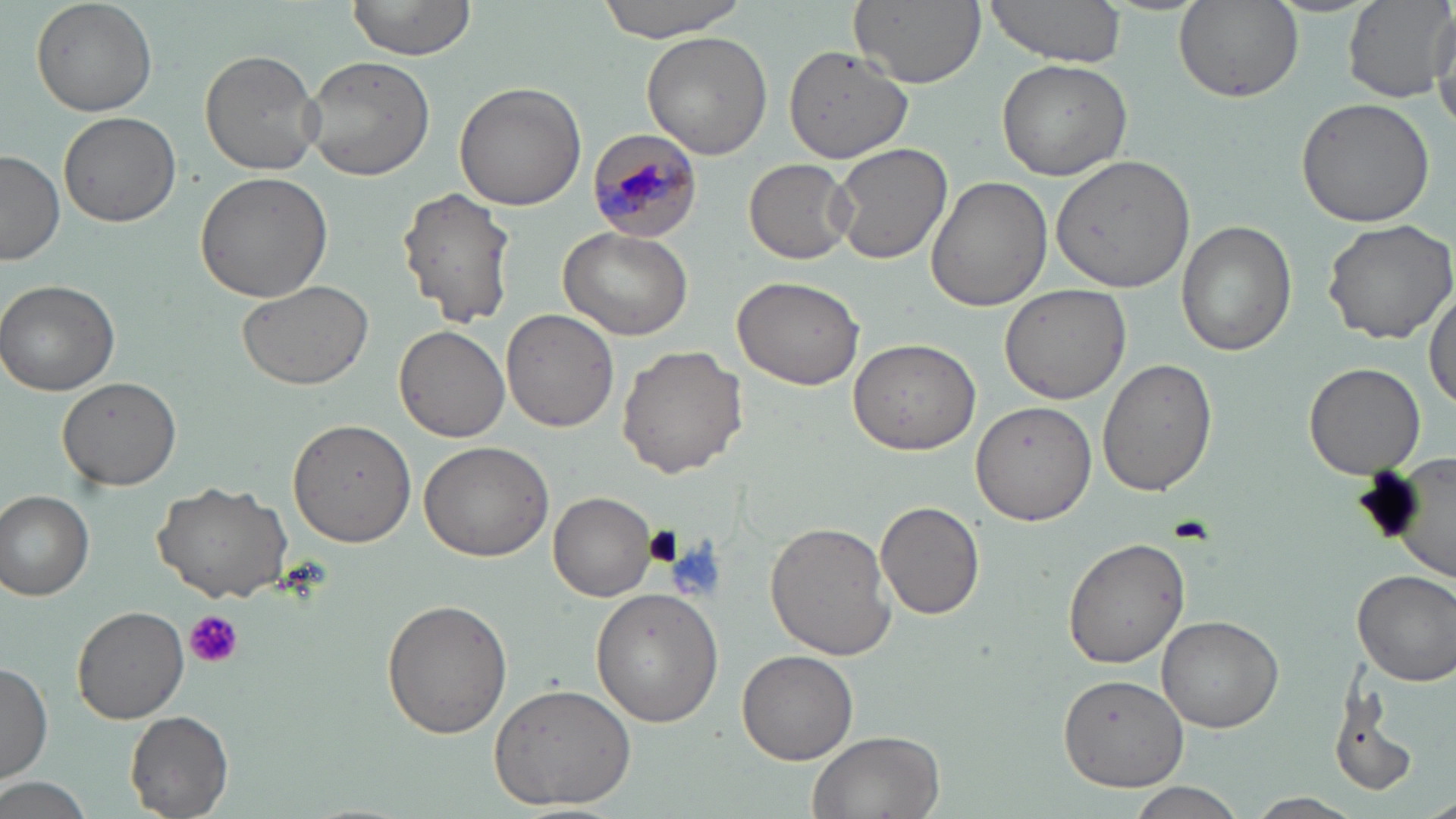

Summary:
  - Coordinate format: approximate bounding boxes as (x1, y1, x2, y2) in pixels
  - Platelet locations: (183, 610, 243, 670)
  - Plasmodium malariae-infected red blood cell locations: (585, 128, 707, 243)
  - Uninfected red blood cell locations: (31, 0, 158, 116), (341, 0, 480, 67), (597, 0, 746, 40), (850, 0, 985, 89), (980, 0, 1129, 66), (1343, 0, 1453, 103), (1174, 1, 1304, 104), (1428, 6, 1456, 124), (641, 30, 772, 159), (785, 44, 913, 166), (199, 49, 324, 176), (301, 56, 435, 182), (996, 58, 1133, 180), (453, 81, 587, 210), (1296, 99, 1435, 226), (59, 110, 182, 227), (830, 142, 953, 265), (0, 149, 64, 265), (1048, 154, 1198, 292), (744, 159, 854, 265), (195, 169, 334, 303), (925, 174, 1052, 312), (396, 186, 516, 328), (1322, 215, 1456, 343), (1175, 220, 1296, 356), (559, 225, 695, 343), (730, 276, 865, 390), (0, 280, 122, 396), (237, 280, 372, 390), (999, 282, 1132, 404), (1426, 284, 1456, 414), (501, 309, 619, 432), (392, 324, 510, 443), (849, 339, 982, 455), (616, 344, 748, 478), (1097, 356, 1217, 496), (1304, 361, 1426, 479), (58, 376, 181, 491), (970, 398, 1097, 526), (288, 418, 418, 548), (419, 440, 554, 562), (1356, 456, 1454, 571), (155, 477, 297, 605), (1, 488, 96, 601), (549, 492, 660, 602), (876, 502, 986, 620), (765, 522, 897, 660), (1062, 534, 1192, 669), (1351, 568, 1456, 686), (591, 589, 724, 728), (381, 599, 514, 739), (73, 604, 191, 724), (1158, 613, 1285, 732), (735, 648, 858, 765), (0, 663, 53, 784), (1057, 671, 1188, 791), (1326, 679, 1419, 802), (488, 684, 638, 810), (126, 711, 233, 818), (806, 728, 947, 819), (1, 776, 91, 819), (1128, 782, 1247, 816), (1422, 789, 1456, 819), (1245, 792, 1364, 818)
  - Slide-level diagnosis: Plasmodium malariae
  - Stain: May-Grünwald-Giemsa
  - Field of view: one of a larger specimen
  - Modality: optical microscopy
  - Preparation: thin blood smear
  - Magnification: 1000x
  - Image size: 1456×819 pixels